Locate every Plasmodium ovale-infected red blood cell.
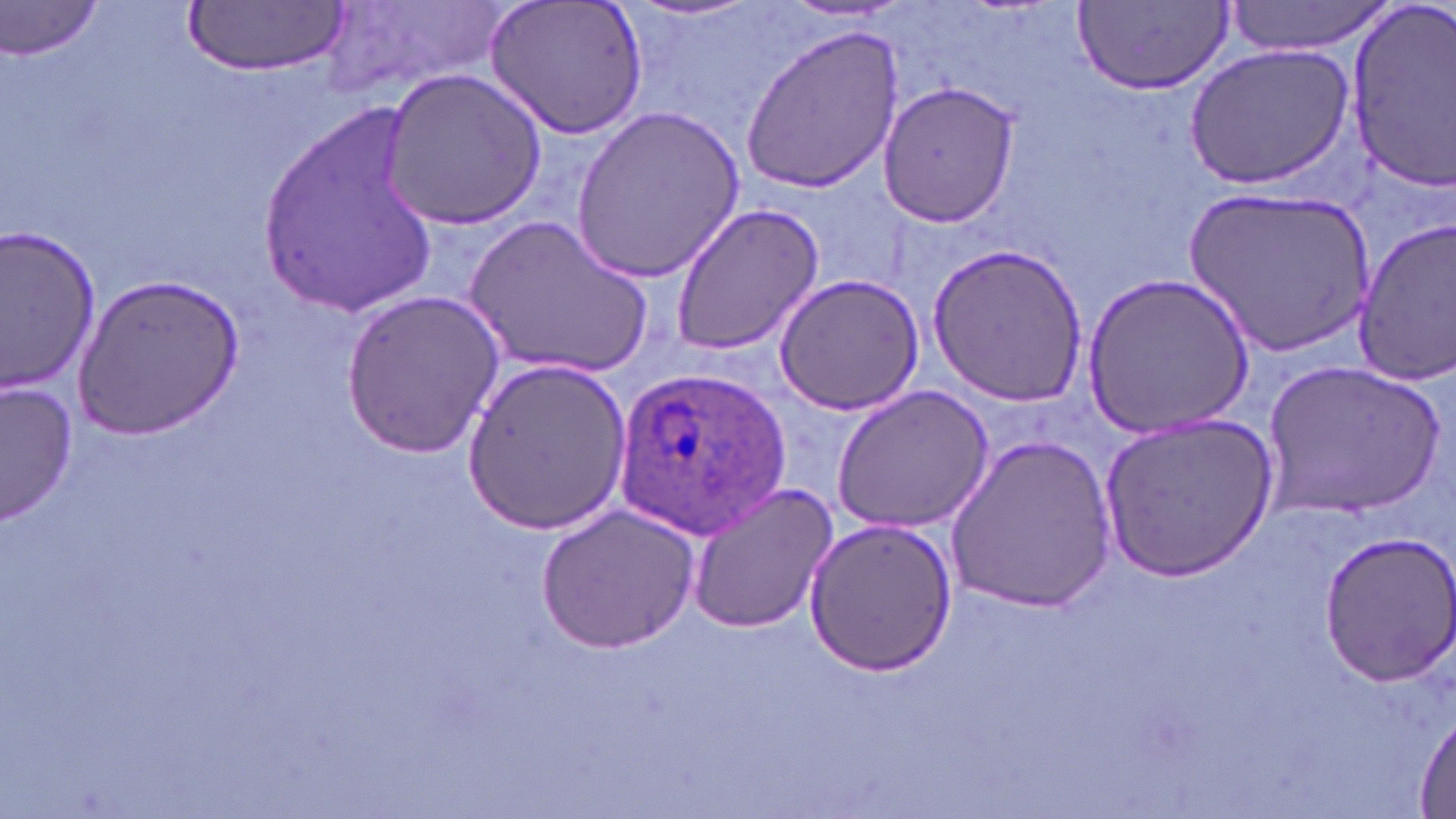

Approximate bounding boxes as (x1,y1)-(x2,y2) corner pairs in pixels.
Plasmodium ovale-infected red blood cells: (615,361)-(793,539).

Uninfected red blood cell locations: (322,0)-(509,103), (484,0)-(649,139), (1223,0)-(1398,57), (0,1)-(109,62), (1072,1)-(1234,92), (182,2)-(348,77), (1339,4)-(1456,191), (740,25)-(907,194), (1181,40)-(1357,192), (379,67)-(548,230), (876,80)-(1021,226), (256,103)-(444,311), (572,103)-(744,283), (1182,183)-(1374,360), (669,202)-(825,356), (466,212)-(656,383), (1352,214)-(1456,386), (0,226)-(101,392), (927,243)-(1091,407), (73,271)-(244,441), (1084,271)-(1254,442), (772,272)-(926,416), (339,289)-(504,459), (466,358)-(631,533), (1262,360)-(1442,518), (2,380)-(78,526), (829,383)-(994,533), (1096,412)-(1275,581), (944,433)-(1117,615), (684,482)-(840,635), (536,504)-(701,655), (801,517)-(958,677), (1316,530)-(1456,688), (1413,709)-(1456,816). Slide-level diagnosis: Plasmodium ovale. May-Grünwald-Giemsa-stained preparation. Optical microscopy. Captured at 1000x magnification. Single field of view. Image is 1456×819 pixels. Thin blood smear.